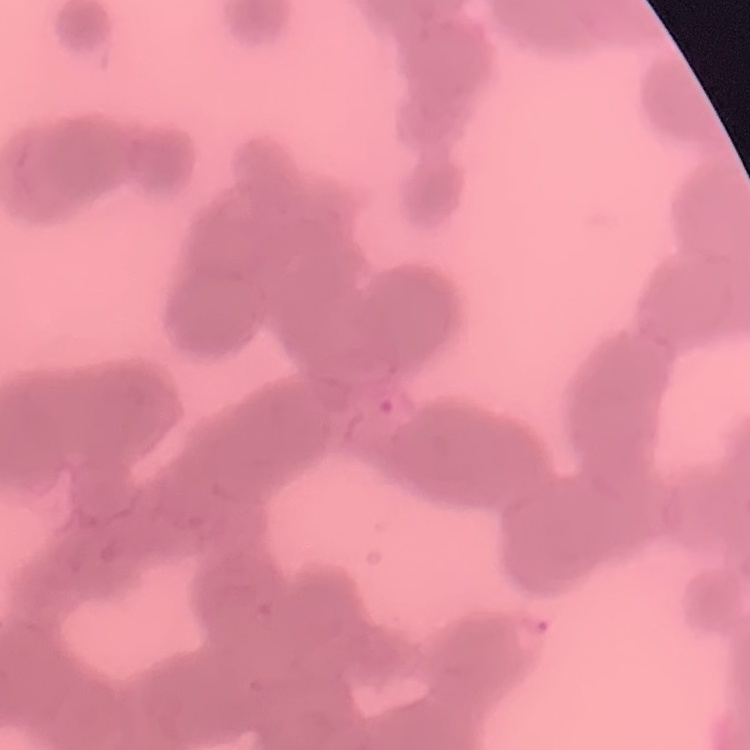
Summary:
  - Erythrocyte morphology: rouleaux formation
  - Stain: Field's or Giemsa
  - Preparation: thin blood smear
  - Image type: square crop of a larger photomicrograph